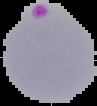
{
  "malaria_status": "parasitized",
  "image_type": "cell region segmented out of the field of view; surrounding area masked to black",
  "preparation": "thin blood film",
  "image_size": "97×106 pixels"
}